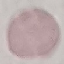
Result: no malaria parasites seen. Giemsa-stained preparation. Cell patch, automatically extracted from a larger field of view and resized to 64 × 64 pixels. Acquired by smartphone through the microscope eyepiece. Thin smear of blood.